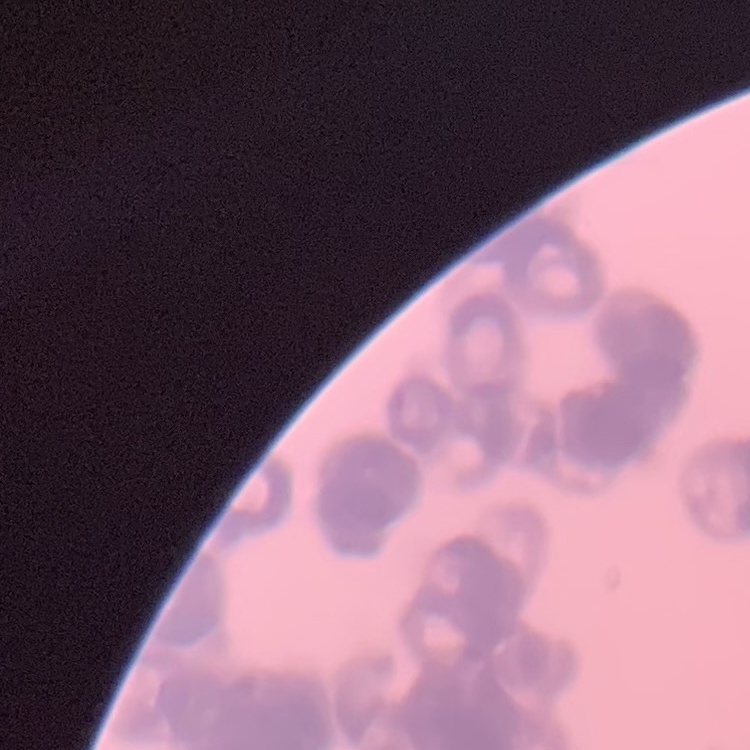

erythrocyte morphology = rouleaux formation
stain = Field's or Giemsa
image type = one tile cut from a larger photomicrograph
preparation = thin blood film